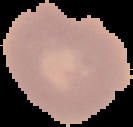

image size = 133×127 pixels
result = no malaria parasites detected
preparation = thin blood film
image type = segmented cell region on a black background